Locate every Plasmodium malariae-infected red blood cell.
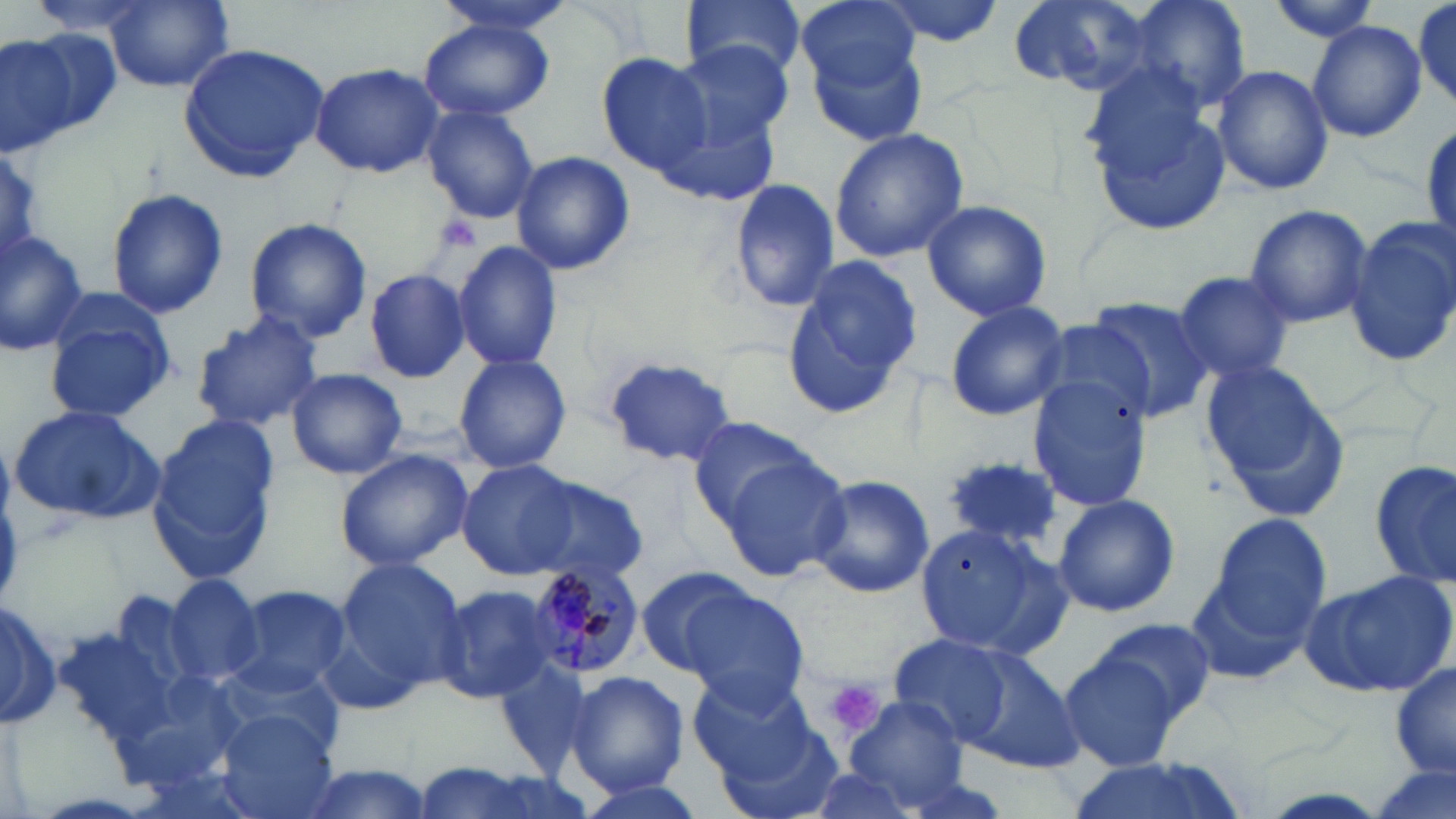
Approximate bounding boxes as (x1,y1)-(x2,y2) corner pairs in pixels.
Plasmodium malariae-infected red blood cells: (526,557)-(648,681).

{
  "slide_level_diagnosis": "Plasmodium malariae",
  "stain": "May-Grünwald-Giemsa",
  "platelet_locations": "approximate bounding boxes as (x1,y1)-(x2,y2) corner pairs in pixels: (430,210)-(482,258), (826,680)-(884,738)",
  "field_of_view": "one of a larger specimen",
  "uninfected_red_blood_cell_locations": "approximate bounding boxes as (x1,y1)-(x2,y2) corner pairs in pixels: (27,0)-(159,40), (428,0)-(579,37), (683,0)-(809,84), (799,0)-(924,99), (874,0)-(1007,49), (1009,0)-(1155,95), (1125,0)-(1252,117), (1263,0)-(1386,44), (105,2)-(233,92), (1414,3)-(1453,106), (420,20)-(552,122), (1310,20)-(1427,142), (807,26)-(931,150), (2,30)-(117,152), (670,40)-(796,152), (178,44)-(331,180), (596,50)-(717,179), (309,62)-(444,177), (1213,63)-(1332,195), (1085,69)-(1232,232), (421,106)-(539,224), (662,108)-(779,207), (829,128)-(969,263), (0,149)-(48,262), (510,151)-(635,276), (730,177)-(840,313), (107,188)-(228,319), (920,199)-(1052,320), (1241,204)-(1373,327), (244,218)-(372,343), (1346,218)-(1456,366), (0,232)-(96,357), (453,240)-(564,370), (781,256)-(921,419), (364,268)-(472,383), (1172,268)-(1295,385), (41,290)-(176,421), (1083,296)-(1217,423), (943,299)-(1069,420), (188,311)-(323,433), (453,351)-(573,473), (602,357)-(738,465), (1202,359)-(1347,517), (286,368)-(408,479), (1025,369)-(1154,510), (9,405)-(165,526), (686,414)-(828,530), (148,416)-(282,584), (334,449)-(473,570), (719,453)-(850,584), (943,454)-(1066,557), (459,460)-(582,577), (1371,463)-(1455,588), (804,473)-(936,600), (523,476)-(649,585), (1053,493)-(1180,618), (1200,512)-(1334,653), (912,518)-(1070,661), (332,557)-(469,702), (636,564)-(762,681), (1298,570)-(1456,700), (165,576)-(260,689), (436,583)-(557,704), (675,583)-(810,711), (224,584)-(351,697), (0,598)-(59,729), (1094,618)-(1216,722), (55,625)-(178,749), (887,635)-(1018,749), (940,642)-(1082,771), (1058,650)-(1188,772), (497,657)-(592,778), (1391,662)-(1456,782), (566,671)-(689,794), (689,675)-(820,783), (843,697)-(968,812), (218,708)-(338,818), (713,714)-(845,819), (1066,755)-(1247,819), (1367,759)-(1456,819), (407,761)-(577,819), (291,763)-(438,819), (567,776)-(712,819)",
  "modality": "light microscopy",
  "image_size": "1456×819 pixels",
  "preparation": "thin blood film",
  "magnification": "1000x"
}